Comment on the morphology of the erythrocytes.
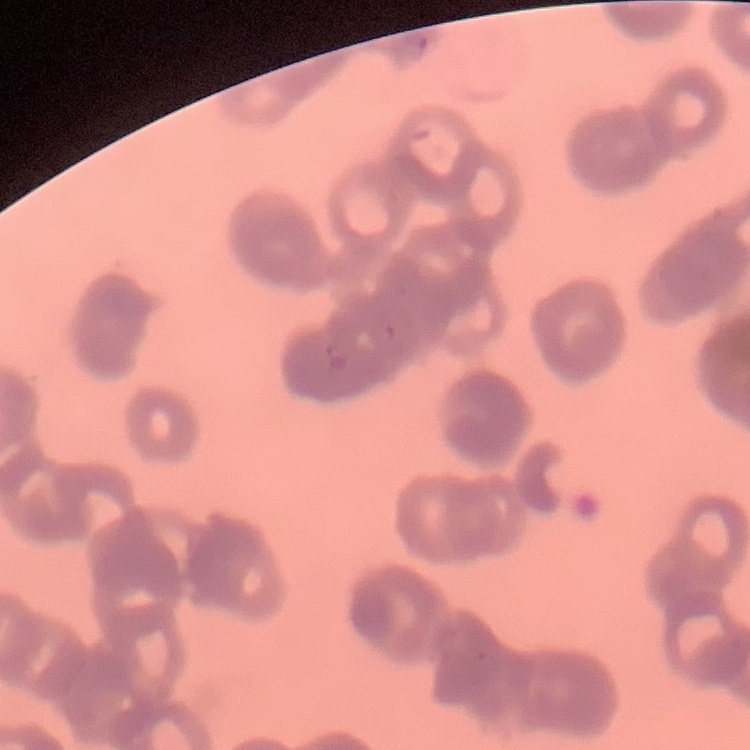
They show rouleaux formation.

Stained with either Field's or Giemsa. Thin blood film. Square crop of a larger photomicrograph.